Point out each leukocyte.
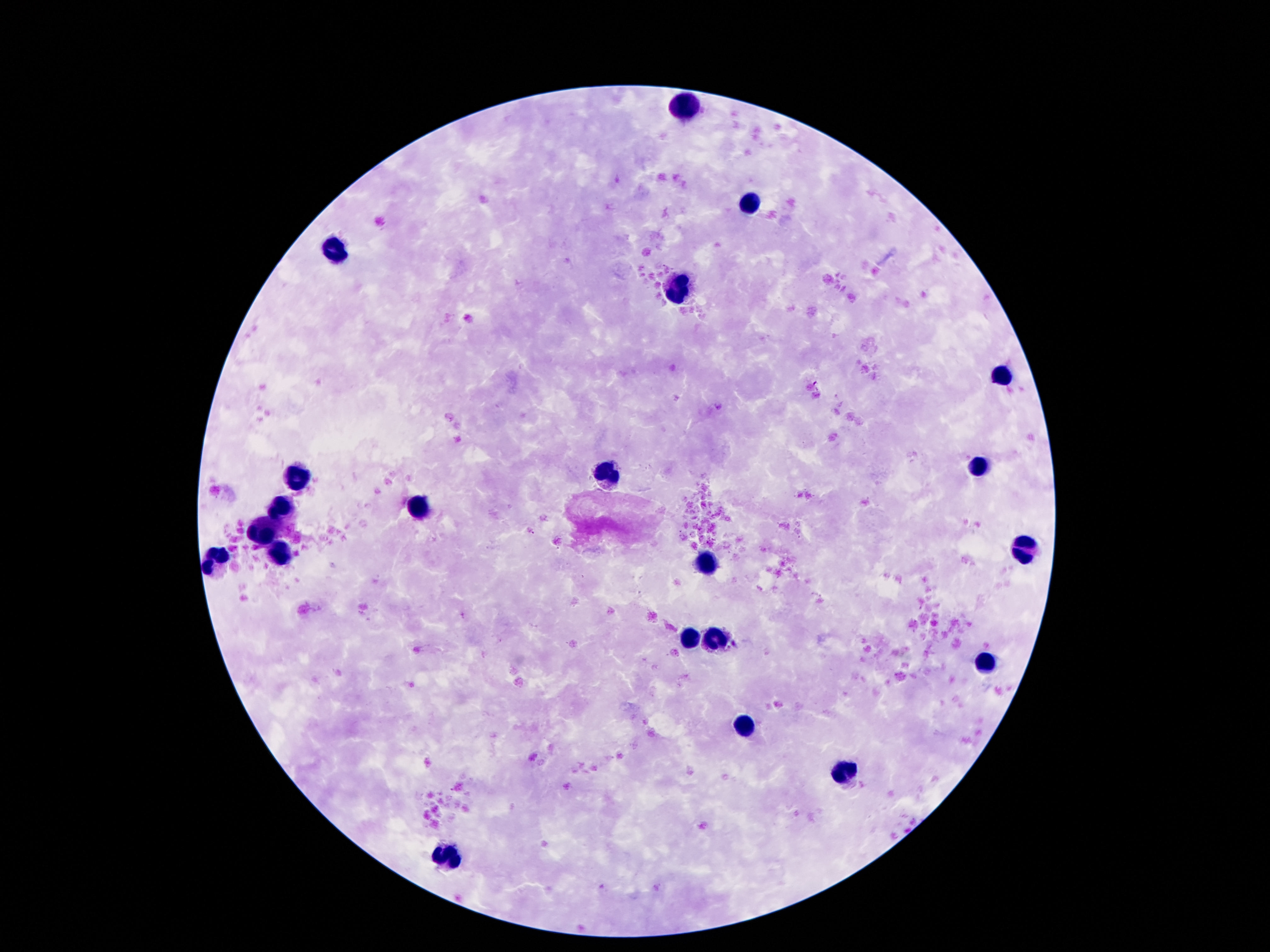
Approximate centers as (x, y) in pixels.
Leukocytes: (686, 106), (749, 201), (334, 249), (674, 294), (1001, 374), (979, 468), (608, 476), (297, 478), (420, 509), (281, 511), (264, 534), (1026, 550), (281, 552), (706, 560), (215, 562), (692, 634), (719, 639), (985, 665), (745, 724), (846, 770), (446, 850).

Summary:
  - Preparation: thick peripheral-blood smear
  - Patient malaria status: negative
  - Field of view: single
  - Stain: Giemsa
  - Capture: smartphone camera through the microscope eyepiece
  - Image size: 1270×952 pixels
  - Magnification: 100x